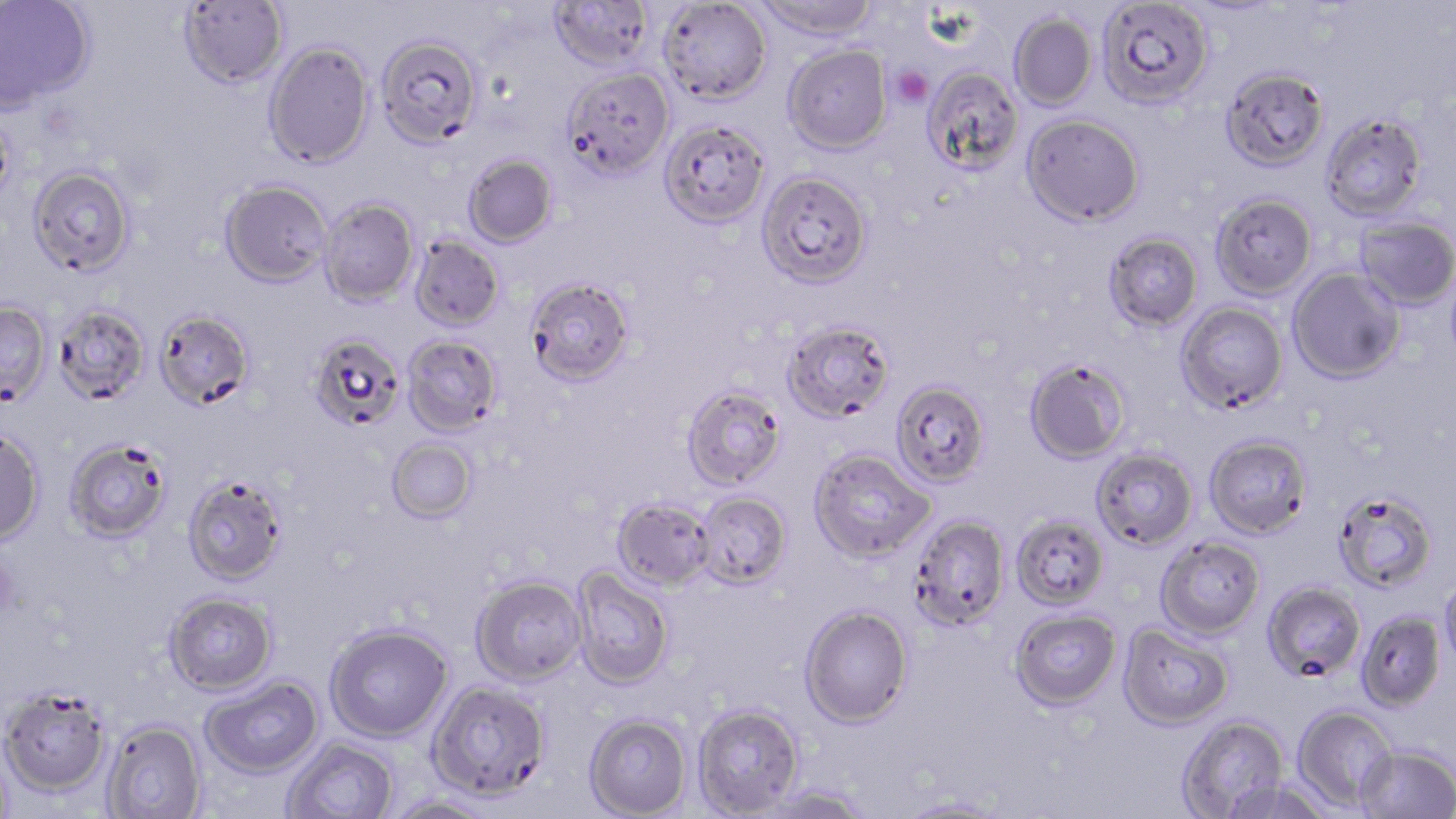

Approximate bounding boxes as named x1/y1/x2/y2 corners in pixels. Uninfected red blood cell locations: (x1=0, y1=0, x2=95, y2=110), (x1=548, y1=0, x2=655, y2=72), (x1=753, y1=0, x2=879, y2=42), (x1=1096, y1=0, x2=1213, y2=109), (x1=178, y1=1, x2=288, y2=89), (x1=659, y1=1, x2=772, y2=104), (x1=1009, y1=13, x2=1098, y2=111), (x1=375, y1=35, x2=482, y2=149), (x1=264, y1=41, x2=374, y2=169), (x1=783, y1=44, x2=892, y2=154), (x1=921, y1=65, x2=1024, y2=174), (x1=1221, y1=66, x2=1329, y2=171), (x1=562, y1=67, x2=674, y2=180), (x1=0, y1=110, x2=16, y2=213), (x1=1320, y1=112, x2=1428, y2=222), (x1=1021, y1=113, x2=1145, y2=227), (x1=659, y1=119, x2=770, y2=228), (x1=463, y1=154, x2=558, y2=249), (x1=28, y1=165, x2=135, y2=276), (x1=757, y1=170, x2=873, y2=289), (x1=220, y1=179, x2=332, y2=287), (x1=1210, y1=193, x2=1318, y2=300), (x1=318, y1=198, x2=418, y2=307), (x1=1355, y1=216, x2=1456, y2=310), (x1=1103, y1=232, x2=1203, y2=331), (x1=410, y1=235, x2=504, y2=332), (x1=1287, y1=267, x2=1405, y2=384), (x1=525, y1=277, x2=635, y2=386), (x1=0, y1=301, x2=53, y2=406), (x1=1175, y1=301, x2=1288, y2=413), (x1=53, y1=304, x2=150, y2=405), (x1=154, y1=308, x2=255, y2=410), (x1=782, y1=320, x2=896, y2=423), (x1=308, y1=333, x2=405, y2=431), (x1=402, y1=335, x2=503, y2=437), (x1=1023, y1=357, x2=1131, y2=464), (x1=891, y1=380, x2=991, y2=488), (x1=681, y1=384, x2=788, y2=489), (x1=0, y1=426, x2=45, y2=546), (x1=1204, y1=434, x2=1313, y2=539), (x1=64, y1=437, x2=172, y2=542), (x1=386, y1=438, x2=478, y2=524), (x1=809, y1=448, x2=936, y2=562), (x1=1091, y1=448, x2=1198, y2=550), (x1=183, y1=474, x2=287, y2=585), (x1=1333, y1=489, x2=1438, y2=593), (x1=695, y1=491, x2=792, y2=589), (x1=611, y1=497, x2=715, y2=591), (x1=1011, y1=513, x2=1109, y2=611), (x1=908, y1=514, x2=1010, y2=630), (x1=1155, y1=536, x2=1265, y2=640), (x1=571, y1=567, x2=673, y2=689), (x1=1439, y1=574, x2=1456, y2=672), (x1=471, y1=576, x2=587, y2=685), (x1=1262, y1=582, x2=1366, y2=683), (x1=164, y1=591, x2=277, y2=695), (x1=799, y1=605, x2=913, y2=728), (x1=1009, y1=608, x2=1122, y2=710), (x1=1355, y1=610, x2=1446, y2=712), (x1=1118, y1=623, x2=1233, y2=730), (x1=325, y1=624, x2=453, y2=742), (x1=200, y1=676, x2=324, y2=778), (x1=427, y1=681, x2=551, y2=802), (x1=0, y1=686, x2=110, y2=796), (x1=692, y1=704, x2=803, y2=817), (x1=1292, y1=705, x2=1397, y2=811), (x1=584, y1=713, x2=691, y2=818), (x1=1175, y1=714, x2=1290, y2=818), (x1=102, y1=720, x2=206, y2=819), (x1=282, y1=738, x2=397, y2=819), (x1=1355, y1=744, x2=1456, y2=819), (x1=1222, y1=777, x2=1335, y2=818), (x1=757, y1=785, x2=871, y2=818), (x1=383, y1=796, x2=502, y2=819), (x1=896, y1=797, x2=1013, y2=818). Platelet locations: (x1=890, y1=65, x2=934, y2=106). Slide-level diagnosis: Plasmodium falciparum. One field of a larger specimen. Optical microscopy. Image is 1456×819 pixels. Captured at 1000x magnification. May-Grünwald-Giemsa stain. Thin blood smear.